Locate every Plasmodium ovale-infected red blood cell.
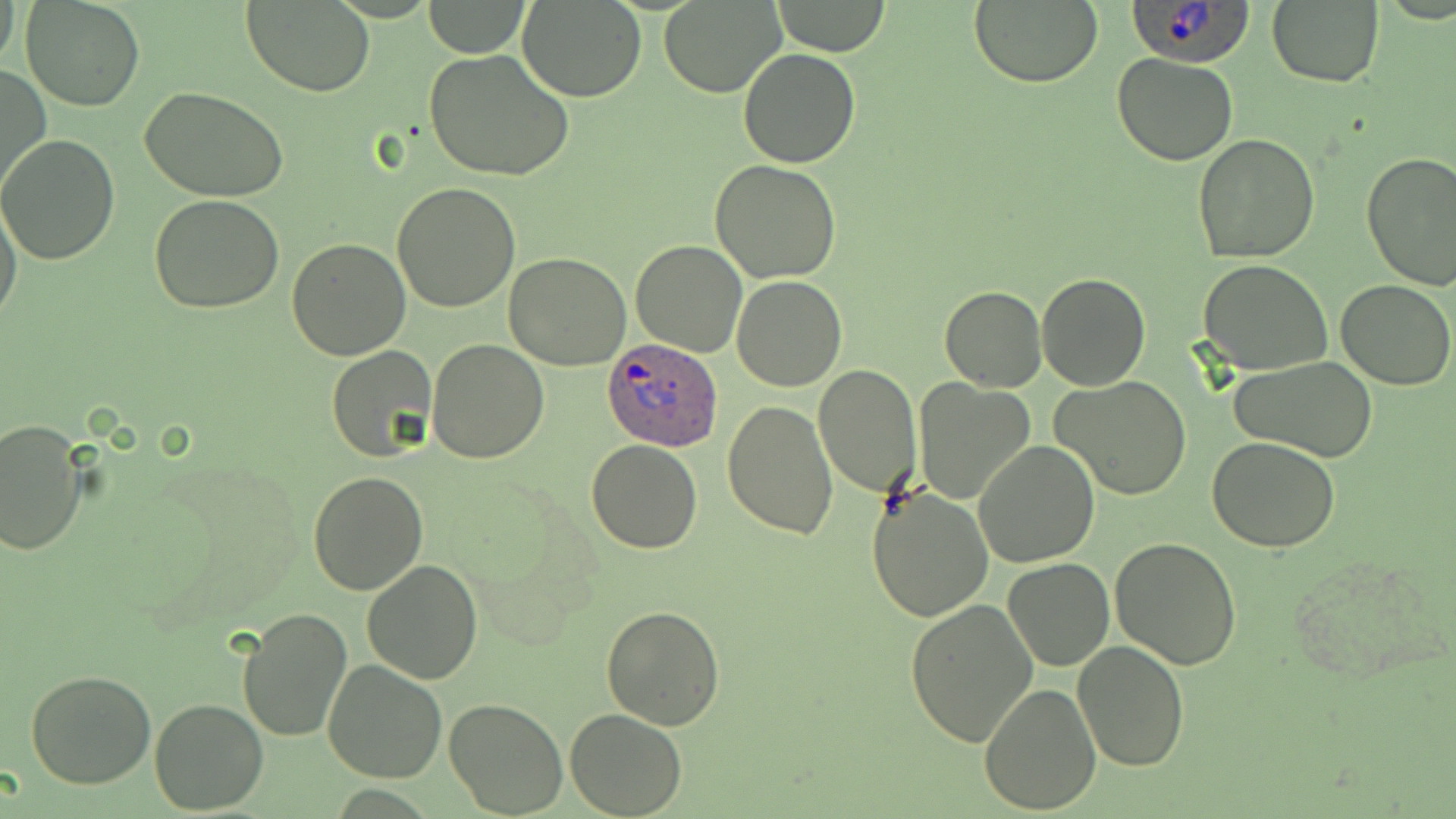

Approximate bounding boxes as (x1, y1, x2, y2) in pixels.
Plasmodium ovale-infected red blood cells: (1126, 0, 1258, 65), (602, 335, 726, 449).

Summary:
  - Uninfected red blood cell locations: (0, 0, 22, 73), (423, 0, 531, 56), (517, 0, 646, 102), (244, 1, 375, 97), (659, 1, 785, 97), (770, 1, 891, 55), (969, 1, 1103, 87), (21, 2, 144, 112), (1267, 2, 1384, 87), (425, 47, 574, 182), (737, 47, 859, 168), (1113, 51, 1237, 165), (0, 65, 50, 198), (141, 87, 291, 201), (1193, 133, 1322, 264), (0, 135, 122, 265), (1360, 151, 1456, 292), (709, 159, 842, 283), (391, 182, 520, 313), (1, 195, 24, 330), (149, 195, 284, 313), (285, 238, 411, 360), (630, 240, 748, 356), (504, 252, 633, 370), (1197, 258, 1333, 374), (1037, 272, 1151, 391), (732, 275, 847, 392), (1335, 278, 1455, 389), (1046, 281, 1173, 481), (940, 285, 1046, 392), (427, 338, 548, 463), (326, 345, 438, 463), (1226, 356, 1381, 459), (813, 365, 922, 499), (1050, 374, 1193, 500), (914, 380, 1035, 503), (721, 399, 838, 539), (0, 419, 89, 557), (1206, 437, 1342, 552), (586, 439, 703, 554), (974, 440, 1099, 567), (308, 470, 429, 595), (867, 485, 995, 624), (1109, 536, 1242, 668), (1004, 557, 1114, 670), (361, 558, 485, 684), (904, 598, 1039, 747), (602, 606, 726, 731), (236, 608, 353, 742), (1073, 639, 1190, 771), (322, 659, 448, 784), (26, 670, 157, 789), (978, 680, 1103, 814), (150, 698, 269, 815), (443, 698, 568, 818), (566, 707, 686, 818)
  - Slide-level diagnosis: Plasmodium ovale
  - Modality: optical microscopy
  - Stain: May-Grünwald-Giemsa
  - Image size: 1456×819 pixels
  - Field of view: single
  - Preparation: thin blood film
  - Magnification: 1000x